Report the malaria status of this cell.
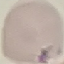
Uninfected.

preparation = thin blood film
image type = cell patch, automatically extracted from a larger field of view and resized to 64 × 64 pixels
capture = smartphone camera at the microscope eyepiece
stain = Giemsa